Classify this cell by malaria status.
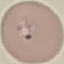

It is uninfected.

image type = cell patch, automatically extracted from a larger field of view and resized to 64 × 64 pixels
preparation = thin blood film
capture = smartphone camera at the microscope eyepiece
stain = Giemsa